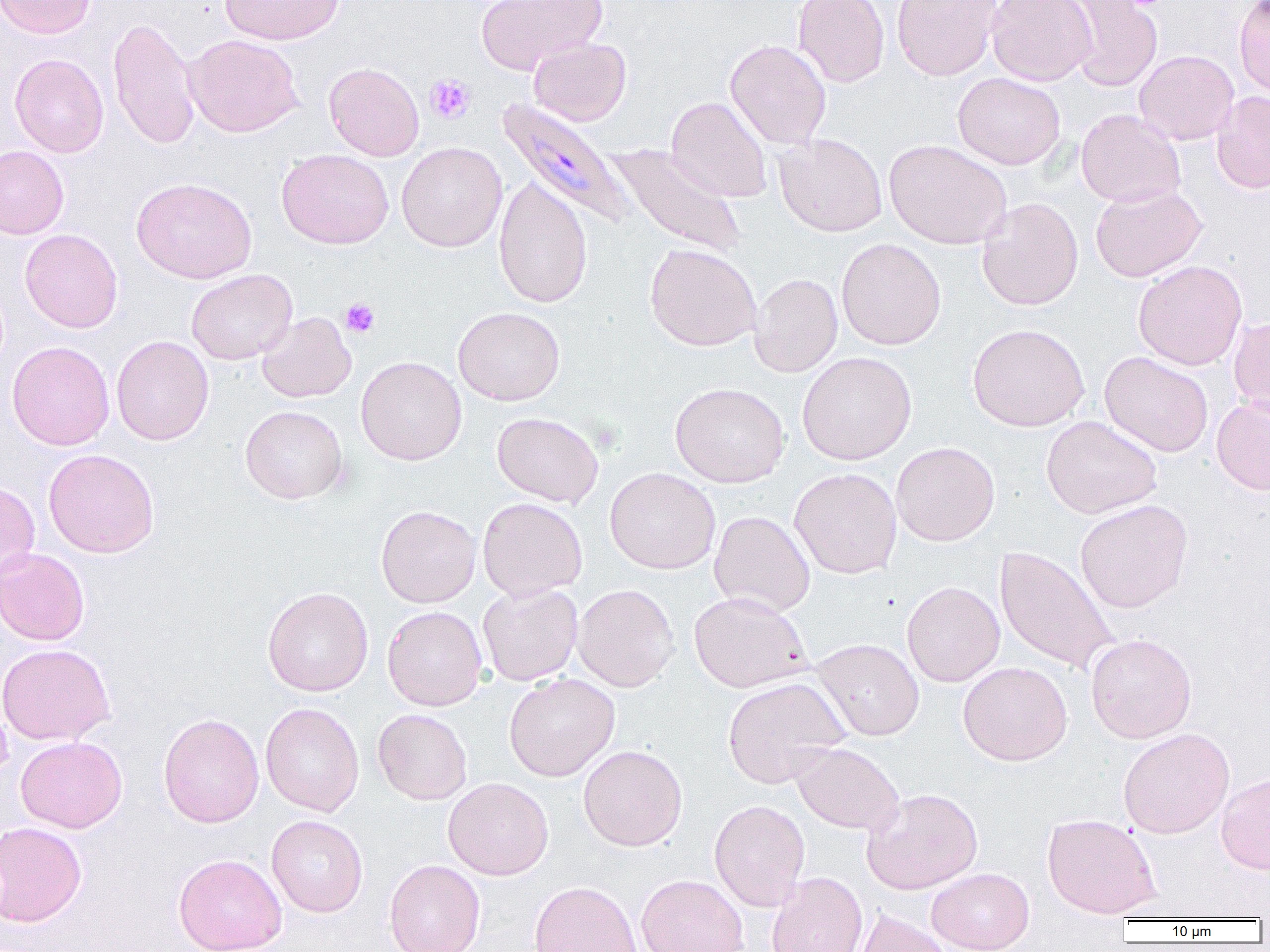

{
  "plasmodium_malariae_infected_red_blood_cell_locations": "approximate bounding boxes as [x1, y1, x2, y2] in pixels: [497, 97, 635, 229]",
  "slide_level_diagnosis": "Plasmodium malariae",
  "platelet_locations": "approximate bounding boxes as [x1, y1, x2, y2] in pixels: [1121, 0, 1168, 10], [425, 74, 475, 124], [340, 298, 380, 338]",
  "field_of_view": "single",
  "uninfected_red_blood_cell_locations": "approximate bounding boxes as [x1, y1, x2, y2] in pixels: [0, 0, 96, 39], [220, 0, 345, 45], [476, 0, 607, 74], [793, 0, 890, 87], [892, 0, 1001, 80], [987, 0, 1098, 85], [1058, 0, 1164, 92], [1233, 0, 1270, 98], [108, 17, 201, 149], [184, 34, 303, 137], [528, 37, 631, 126], [725, 40, 831, 149], [1134, 50, 1239, 145], [10, 54, 109, 158], [324, 62, 424, 160], [953, 72, 1066, 170], [1211, 91, 1270, 194], [666, 96, 773, 203], [1076, 109, 1186, 208], [774, 132, 887, 237], [884, 139, 1012, 249], [396, 141, 507, 252], [608, 143, 747, 259], [0, 146, 69, 239], [276, 148, 394, 249], [131, 177, 257, 284], [493, 177, 594, 309], [1090, 184, 1207, 282], [976, 197, 1084, 311], [20, 229, 123, 333], [836, 237, 946, 350], [644, 243, 762, 351], [1132, 260, 1248, 371], [186, 269, 297, 365], [749, 273, 843, 377], [453, 306, 565, 406], [257, 311, 356, 403], [1228, 316, 1270, 419], [967, 323, 1089, 432], [111, 335, 214, 446], [7, 341, 115, 451], [796, 351, 917, 465], [1099, 351, 1214, 457], [356, 355, 467, 465], [669, 382, 790, 488], [1211, 395, 1270, 495], [240, 405, 349, 504], [492, 411, 604, 507], [1040, 415, 1162, 518], [891, 441, 1000, 546], [43, 448, 160, 558], [605, 467, 720, 574], [789, 467, 902, 579], [0, 481, 40, 584], [477, 497, 588, 601], [1074, 499, 1194, 613], [375, 505, 481, 607], [708, 510, 815, 616], [994, 545, 1119, 676], [0, 547, 90, 646], [901, 581, 1005, 687], [477, 583, 583, 686], [572, 583, 680, 692], [262, 587, 374, 696], [688, 590, 813, 693], [382, 605, 488, 711], [1085, 633, 1197, 743], [811, 638, 925, 741], [0, 643, 115, 746], [958, 661, 1073, 765], [504, 673, 620, 782], [722, 676, 849, 788], [260, 702, 365, 817], [373, 708, 472, 805], [158, 713, 264, 828], [1118, 727, 1235, 838], [15, 736, 127, 833], [791, 741, 905, 834], [578, 744, 688, 851], [1216, 772, 1270, 874], [442, 777, 554, 880], [861, 787, 983, 893], [709, 799, 811, 911], [1041, 813, 1161, 918], [266, 815, 368, 917], [0, 821, 87, 927], [200, 826, 352, 931], [174, 853, 287, 952], [384, 859, 485, 952], [926, 867, 1035, 951], [766, 871, 867, 952], [636, 874, 749, 952], [528, 881, 642, 952], [854, 908, 952, 952]",
  "modality": "light microscopy",
  "preparation": "thin blood film",
  "image_size": "1270×952 pixels",
  "magnification": "1000x"
}